State which parasite is depicted.
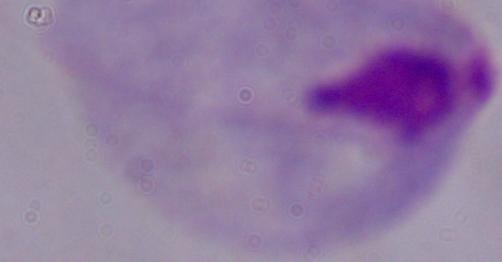

A trichomonad.

1000x magnification. Micrograph.